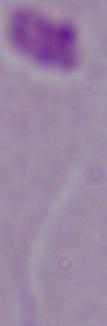

A Leishmania parasite is shown. Captured at 1000x magnification. Micrograph.